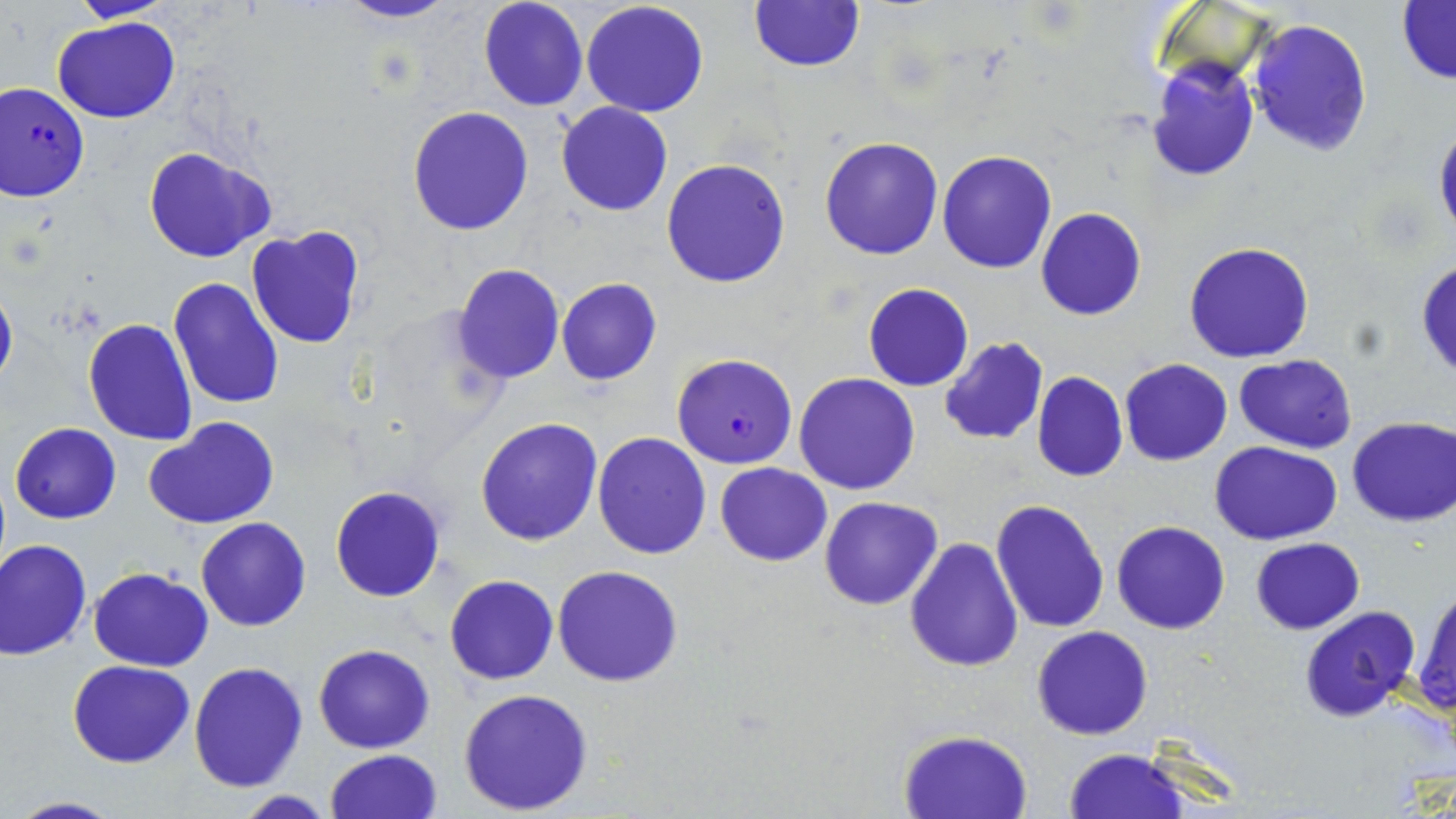
Approximate bounding boxes as (x1,y1)-(x2,y2) corner pairs in pixels. Uninfected red blood cell locations: (71,0)-(174,23), (333,0)-(461,25), (477,0)-(589,112), (581,1)-(709,118), (747,1)-(867,73), (1396,2)-(1456,83), (52,17)-(182,123), (1247,18)-(1373,157), (1147,59)-(1259,183), (556,103)-(673,217), (406,105)-(533,234), (1433,122)-(1455,242), (819,135)-(945,260), (144,147)-(275,262), (936,150)-(1058,273), (661,158)-(791,288), (1037,208)-(1145,321), (247,226)-(364,350), (1184,242)-(1314,364), (1416,257)-(1456,382), (453,263)-(564,383), (168,276)-(285,410), (0,278)-(17,395), (556,279)-(661,386), (863,283)-(973,392), (83,317)-(197,446), (938,337)-(1049,445), (1234,354)-(1359,452), (1120,359)-(1232,466), (1032,371)-(1127,482), (794,372)-(922,495), (476,416)-(603,546), (143,417)-(278,530), (1346,417)-(1455,526), (10,422)-(121,523), (591,431)-(710,560), (1210,441)-(1344,546), (715,463)-(832,566), (329,485)-(446,602), (820,496)-(942,610), (990,499)-(1110,632), (195,517)-(312,632), (1112,521)-(1230,634), (904,535)-(1024,672), (1249,537)-(1364,634), (0,539)-(92,659), (552,565)-(684,687), (88,567)-(214,671), (446,575)-(559,685), (1412,586)-(1456,715), (1297,606)-(1422,722), (1031,625)-(1153,741), (314,643)-(434,753), (68,658)-(196,767), (188,662)-(307,792), (459,687)-(594,815), (899,729)-(1032,817), (1064,748)-(1188,819), (325,750)-(441,819), (233,792)-(340,819), (7,797)-(123,818). Plasmodium falciparum-infected red blood cell locations: (0,82)-(89,202), (671,352)-(798,468). Slide-level diagnosis: Plasmodium falciparum. Image is 1456×819 pixels. Single field of view. Light microscopy. Captured at 1000x magnification. May-Grünwald-Giemsa-stained preparation. Thin blood film.